State which parasite is depicted.
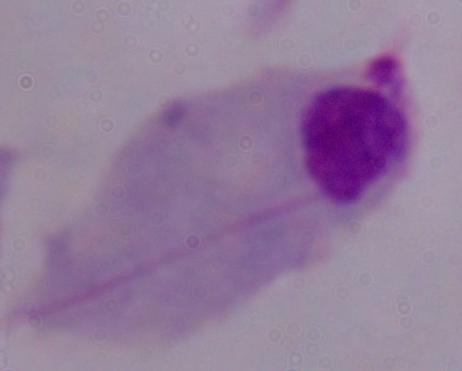
This is a trichomonad.

magnification = 1000x
modality = micrograph